Locate and identify every blood parasite.
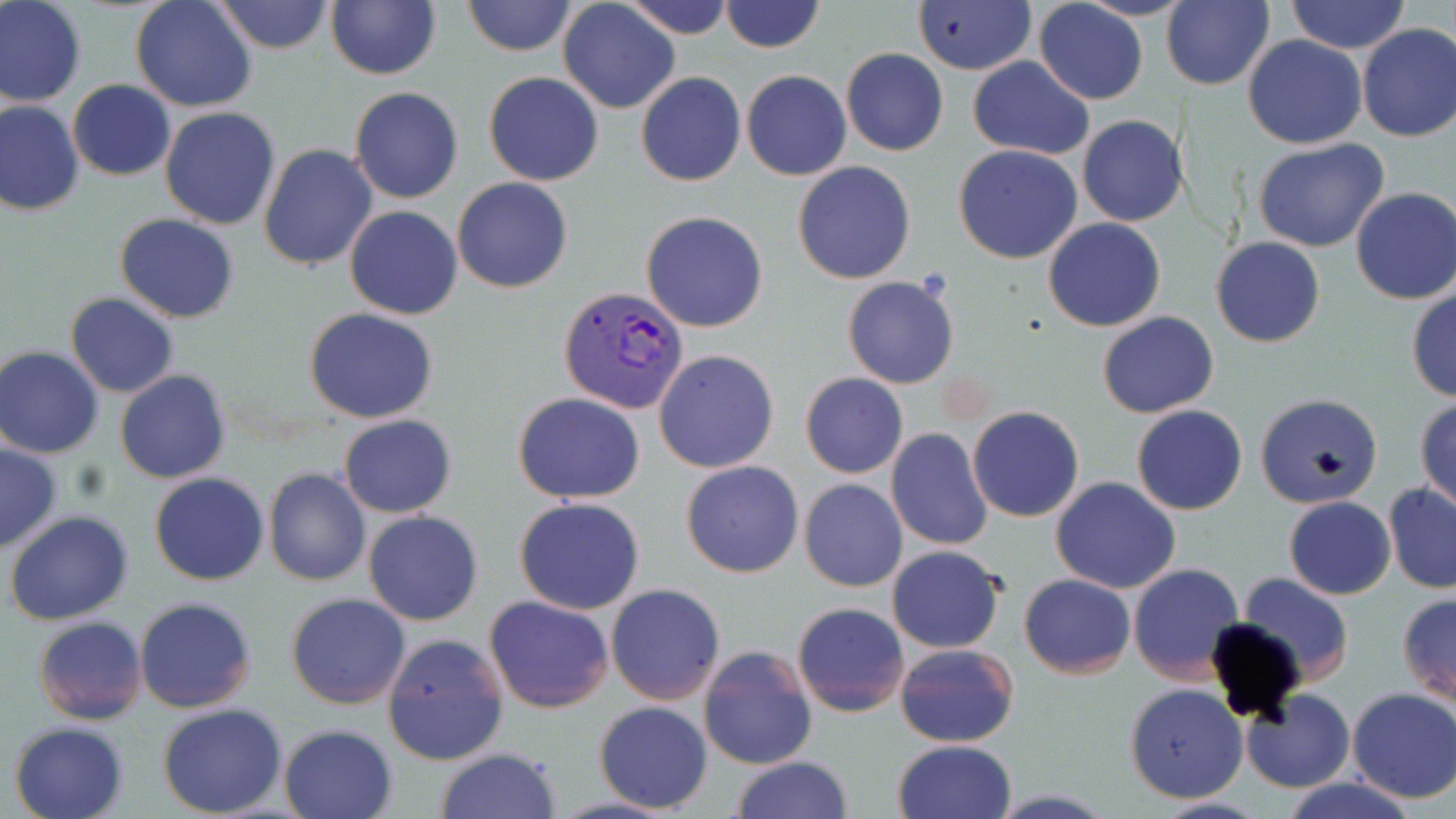
Approximate bounding boxes as named x1/y1/x2/y2 corners in pixels.
Plasmodium vivax-infected red blood cells: (x1=559, y1=285, x2=691, y2=416).
No Plasmodium falciparum, Plasmodium ovale, Plasmodium malariae, Babesia divergens, or Trypanosoma brucei observed.

Uninfected red blood cell locations: (x1=0, y1=0, x2=87, y2=108), (x1=130, y1=0, x2=258, y2=113), (x1=212, y1=0, x2=336, y2=54), (x1=619, y1=0, x2=735, y2=40), (x1=719, y1=0, x2=824, y2=53), (x1=912, y1=0, x2=1035, y2=75), (x1=1078, y1=0, x2=1190, y2=21), (x1=462, y1=1, x2=578, y2=56), (x1=1034, y1=1, x2=1148, y2=103), (x1=1164, y1=1, x2=1274, y2=89), (x1=1285, y1=1, x2=1412, y2=54), (x1=326, y1=2, x2=441, y2=80), (x1=558, y1=2, x2=679, y2=114), (x1=1356, y1=22, x2=1456, y2=142), (x1=1242, y1=36, x2=1368, y2=150), (x1=841, y1=47, x2=948, y2=157), (x1=966, y1=57, x2=1093, y2=160), (x1=741, y1=69, x2=852, y2=180), (x1=483, y1=72, x2=604, y2=186), (x1=636, y1=72, x2=745, y2=187), (x1=68, y1=80, x2=176, y2=180), (x1=349, y1=86, x2=464, y2=204), (x1=0, y1=101, x2=83, y2=218), (x1=159, y1=107, x2=281, y2=230), (x1=1064, y1=114, x2=1178, y2=326), (x1=1077, y1=115, x2=1188, y2=226), (x1=1252, y1=138, x2=1392, y2=254), (x1=259, y1=144, x2=379, y2=269), (x1=953, y1=145, x2=1083, y2=264), (x1=792, y1=161, x2=917, y2=284), (x1=452, y1=177, x2=573, y2=293), (x1=1350, y1=186, x2=1456, y2=305), (x1=344, y1=205, x2=462, y2=320), (x1=642, y1=211, x2=767, y2=332), (x1=115, y1=214, x2=238, y2=323), (x1=1043, y1=217, x2=1165, y2=331), (x1=1211, y1=237, x2=1324, y2=348), (x1=843, y1=276, x2=959, y2=389), (x1=1406, y1=285, x2=1456, y2=403), (x1=66, y1=292, x2=179, y2=397), (x1=306, y1=307, x2=437, y2=423), (x1=1097, y1=310, x2=1219, y2=418), (x1=0, y1=347, x2=104, y2=459), (x1=653, y1=349, x2=779, y2=474), (x1=116, y1=370, x2=231, y2=483), (x1=800, y1=372, x2=908, y2=479), (x1=513, y1=392, x2=645, y2=503), (x1=1255, y1=392, x2=1383, y2=508), (x1=1415, y1=399, x2=1456, y2=513), (x1=1132, y1=405, x2=1248, y2=515), (x1=968, y1=406, x2=1083, y2=523), (x1=338, y1=415, x2=456, y2=517), (x1=886, y1=427, x2=992, y2=551), (x1=0, y1=442, x2=63, y2=554), (x1=680, y1=460, x2=803, y2=577), (x1=263, y1=468, x2=370, y2=586), (x1=150, y1=472, x2=269, y2=585), (x1=1049, y1=476, x2=1181, y2=594), (x1=799, y1=478, x2=908, y2=593), (x1=1383, y1=482, x2=1456, y2=594), (x1=1283, y1=496, x2=1396, y2=600), (x1=515, y1=497, x2=645, y2=615), (x1=4, y1=511, x2=133, y2=626), (x1=363, y1=511, x2=483, y2=626), (x1=886, y1=545, x2=1005, y2=653), (x1=1129, y1=563, x2=1245, y2=684), (x1=1018, y1=573, x2=1136, y2=678), (x1=1238, y1=573, x2=1354, y2=682), (x1=605, y1=582, x2=725, y2=703), (x1=287, y1=592, x2=412, y2=710), (x1=1396, y1=593, x2=1456, y2=707), (x1=485, y1=595, x2=614, y2=713), (x1=135, y1=597, x2=256, y2=714), (x1=792, y1=601, x2=909, y2=716), (x1=33, y1=616, x2=148, y2=725), (x1=380, y1=632, x2=511, y2=767), (x1=894, y1=641, x2=1020, y2=748), (x1=698, y1=646, x2=817, y2=770), (x1=1125, y1=683, x2=1248, y2=803), (x1=1346, y1=689, x2=1456, y2=803), (x1=1241, y1=691, x2=1355, y2=793), (x1=594, y1=701, x2=712, y2=814), (x1=157, y1=702, x2=288, y2=818), (x1=8, y1=720, x2=129, y2=819), (x1=278, y1=724, x2=400, y2=819), (x1=892, y1=739, x2=1019, y2=819), (x1=436, y1=747, x2=560, y2=819), (x1=730, y1=756, x2=855, y2=818), (x1=1276, y1=777, x2=1427, y2=819), (x1=1146, y1=797, x2=1271, y2=818). Slide-level diagnosis: Plasmodium vivax. Light microscopy. 1000x magnification. Thin blood smear. May-Grünwald-Giemsa stain. Image is 1456×819 pixels. Single field of view.